Classify this cell by malaria status.
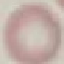

It is uninfected.

{
  "capture": "smartphone through the microscope eyepiece",
  "image_type": "cell patch, automatically extracted from a larger field of view and resized to 64 × 64 pixels",
  "preparation": "thin smear",
  "stain": "Giemsa"
}